Classify this cell by malaria status.
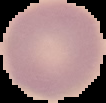

It is uninfected.

image size = 106×103 pixels
preparation = thin blood film
image type = segmented cell region on a black background